Assess the morphology of the erythrocytes.
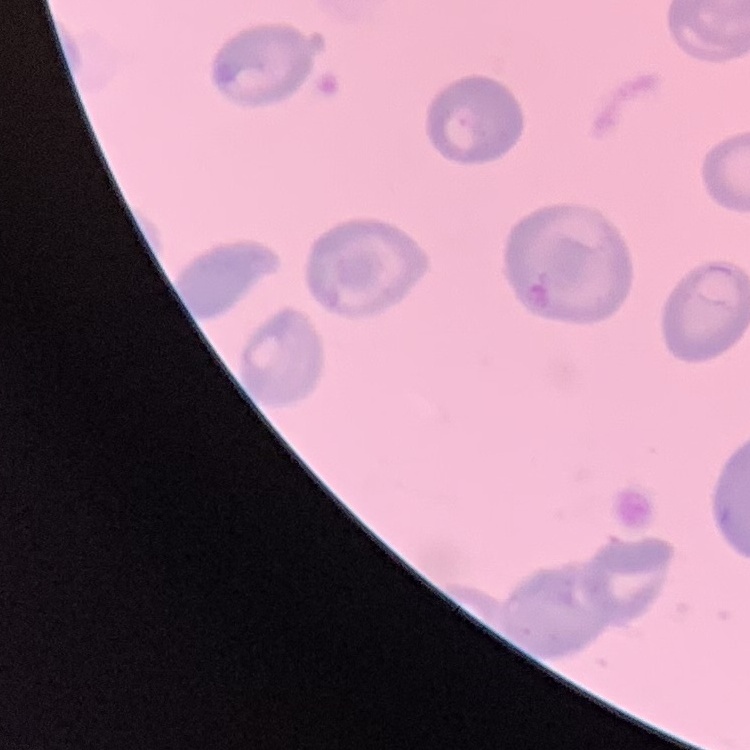

They show no rouleaux formation.

stain: Field's or Giemsa
image_type: one tile cut from a larger photomicrograph
preparation: thin peripheral smear